Name the parasite shown.
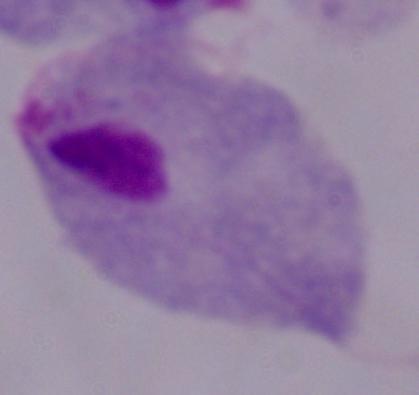

This is a trichomonad.

modality = photomicrograph
magnification = 1000x